Identify the preparation type.
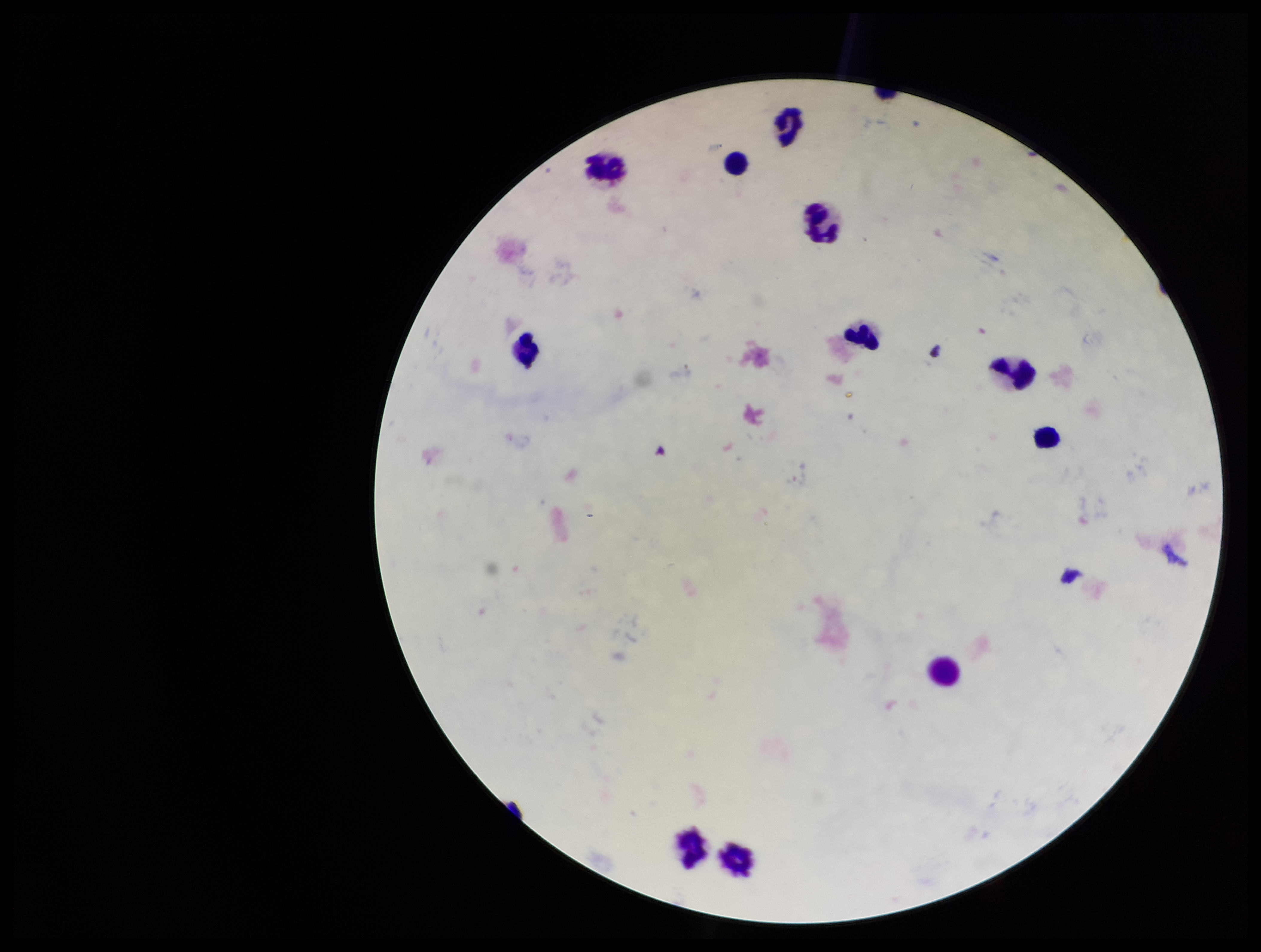
Thick.

Parasite count: 0. Giemsa stain. Image is 1261×952 pixels. Plasmodium parasites: none seen. Single field of view. Leukocyte count: 11. Photographed through the microscope eyepiece with a smartphone camera. Patient malaria status: negative.